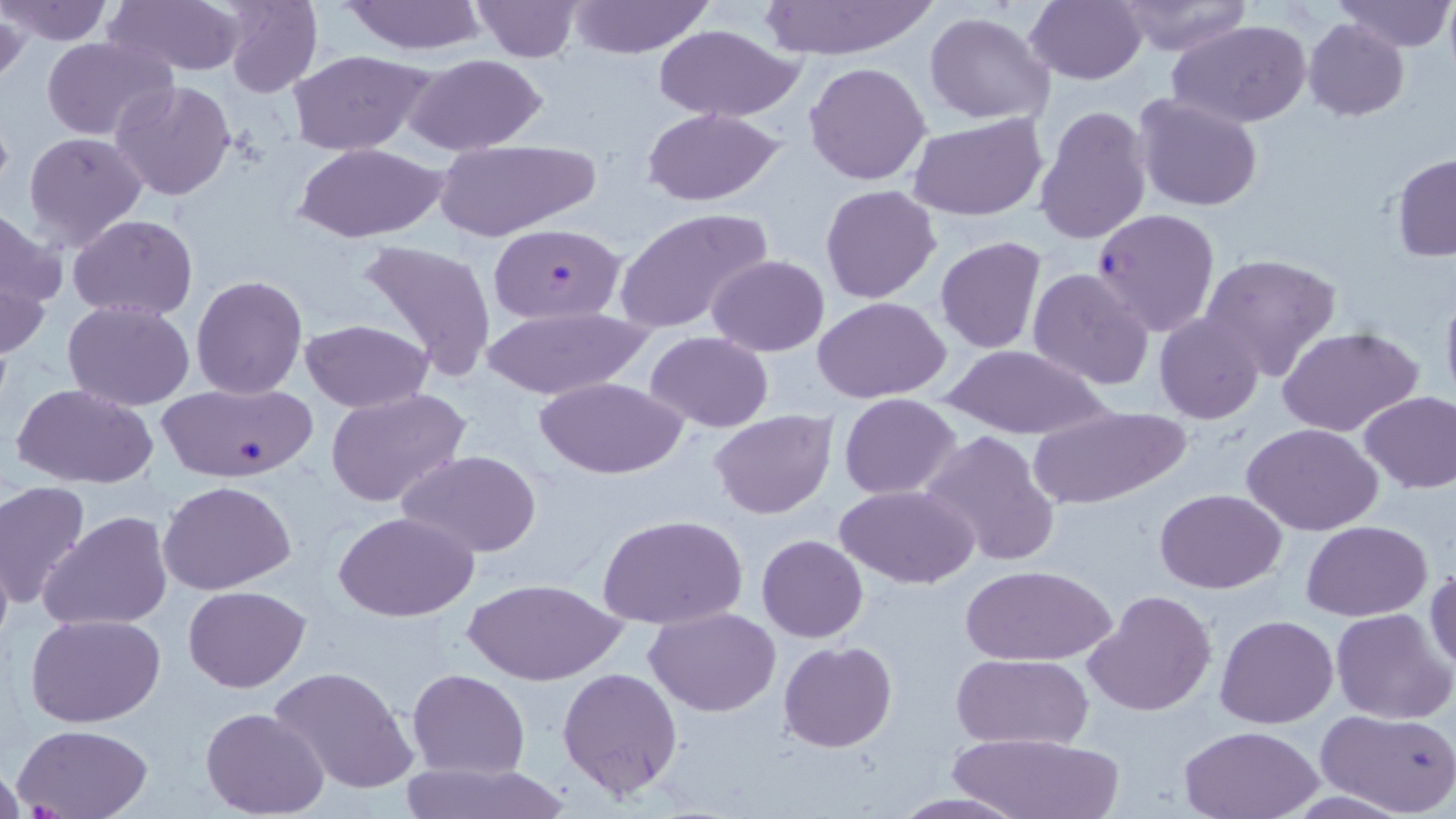 Approximate bounding boxes as [x1, y1, x2, y2] in pixels. Plasmodium falciparum-infected red blood cell locations: [1090, 208, 1219, 338], [485, 224, 625, 323], [157, 380, 317, 483]. Uninfected red blood cell locations: [0, 0, 113, 45], [105, 0, 247, 76], [219, 0, 322, 99], [341, 0, 486, 55], [469, 0, 582, 61], [1024, 0, 1147, 85], [1114, 0, 1253, 56], [1335, 0, 1455, 52], [566, 1, 715, 58], [755, 1, 937, 60], [0, 12, 28, 83], [923, 12, 1055, 126], [1167, 19, 1312, 128], [1303, 19, 1411, 120], [650, 24, 805, 122], [42, 35, 177, 141], [286, 49, 433, 156], [403, 54, 551, 155], [804, 61, 933, 186], [110, 80, 238, 201], [1133, 94, 1263, 213], [1032, 104, 1154, 247], [641, 107, 785, 206], [907, 113, 1047, 222], [22, 130, 148, 251], [432, 138, 601, 239], [295, 142, 448, 241], [1391, 153, 1456, 262], [820, 185, 942, 303], [1, 207, 65, 331], [614, 207, 775, 334], [69, 214, 198, 320], [935, 237, 1047, 353], [357, 238, 497, 382], [0, 248, 52, 368], [1199, 252, 1342, 383], [707, 254, 830, 357], [1027, 266, 1155, 391], [190, 275, 307, 399], [1439, 284, 1456, 415], [813, 298, 953, 401], [64, 301, 195, 412], [481, 305, 653, 400], [1154, 314, 1264, 424], [301, 319, 433, 413], [1278, 325, 1426, 439], [646, 332, 774, 432], [943, 345, 1112, 439], [535, 376, 687, 479], [13, 384, 156, 489], [325, 389, 472, 508], [1358, 390, 1456, 493], [838, 394, 962, 498], [1029, 403, 1192, 512], [709, 409, 837, 519], [1242, 422, 1385, 536], [920, 428, 1061, 568], [396, 450, 543, 558], [157, 480, 296, 595], [0, 481, 93, 611], [834, 484, 978, 588], [1155, 488, 1287, 595], [38, 510, 175, 632], [336, 512, 479, 622], [597, 513, 749, 630], [1302, 519, 1432, 619], [756, 534, 868, 642], [0, 543, 13, 661], [960, 565, 1114, 667], [1426, 569, 1456, 675], [466, 579, 622, 684], [182, 585, 310, 692], [1085, 589, 1217, 717], [646, 607, 781, 715], [1331, 608, 1455, 726], [26, 612, 167, 726], [1215, 614, 1339, 729], [778, 641, 896, 752], [952, 654, 1092, 749], [268, 666, 419, 796], [407, 668, 529, 779], [557, 668, 683, 801], [200, 706, 330, 819], [1316, 707, 1456, 817], [11, 722, 155, 818], [1178, 724, 1324, 818], [949, 731, 1123, 818], [401, 762, 569, 819], [883, 791, 1034, 818]. Slide-level diagnosis: Plasmodium falciparum. Thin blood smear. Image is 1456×819 pixels. Captured at 1000x magnification. May-Grünwald-Giemsa stain. Single field of view. Optical microscopy.